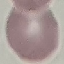

Summary:
  - Malaria status: uninfected
  - Capture: smartphone camera at the microscope eyepiece
  - Image type: cell patch, automatically extracted from a larger field of view and resized to 64 × 64 pixels
  - Preparation: thin smear
  - Stain: Giemsa